Describe the morphology of the red blood cells.
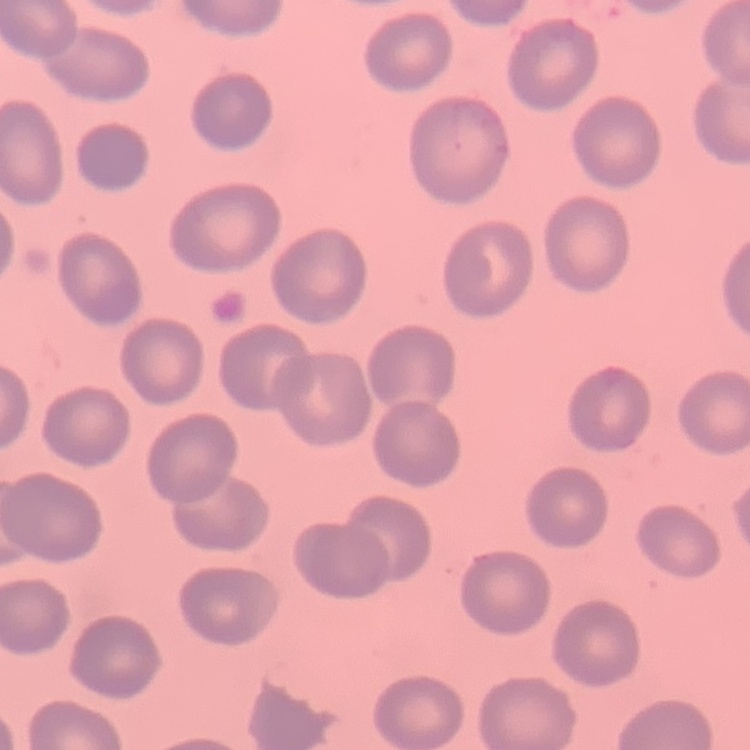
They show no rouleaux formation.

{
  "stain": "Field's or Giemsa",
  "image_type": "one tile cut from a larger photomicrograph",
  "preparation": "thin peripheral smear"
}